Classify this cell by malaria status.
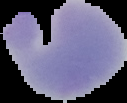
Parasitized.

image type = segmented cell region on a black background
preparation = thin blood film
image size = 127×103 pixels